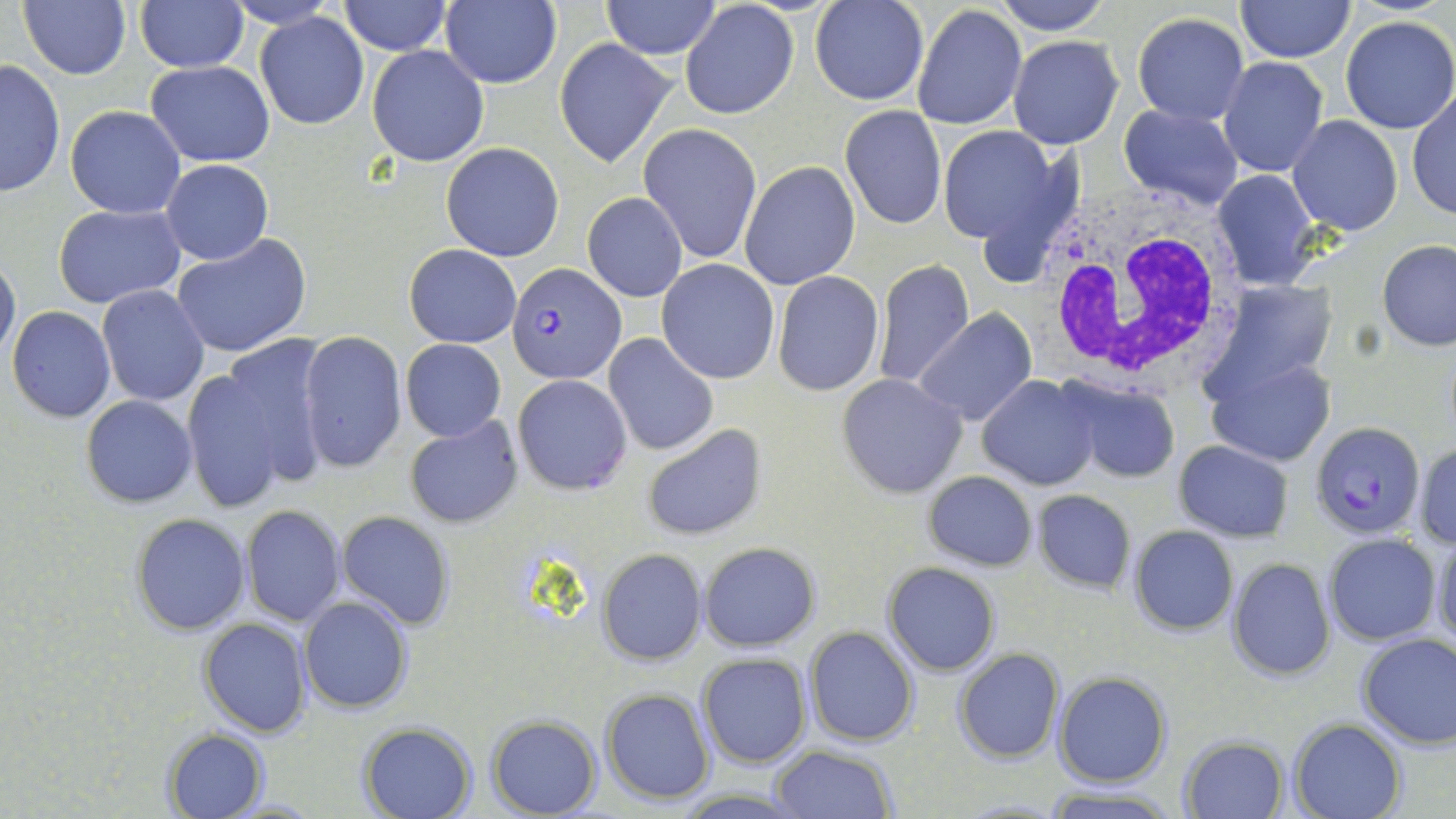
slide-level diagnosis = Plasmodium falciparum
modality = light microscopy
stain = May-Grünwald-Giemsa
field of view = one of a larger specimen
magnification = 1000x
uninfected red blood cell locations = approximate bounding boxes as (x1,y1)-(x2,y2) corner pairs in pixels: (18,0)-(131,80), (341,0)-(451,54), (439,0)-(562,89), (600,0)-(723,59), (810,0)-(928,104), (995,0)-(1112,34), (1236,0)-(1353,62), (135,1)-(249,73), (681,5)-(796,120), (912,5)-(1028,131), (1131,12)-(1248,126), (255,13)-(369,129), (1338,16)-(1456,135), (1007,36)-(1124,150), (554,39)-(676,169), (367,44)-(489,167), (1216,55)-(1329,178), (1,58)-(64,198), (147,62)-(274,165), (1406,90)-(1455,223), (1119,102)-(1244,209), (64,105)-(187,218), (840,105)-(946,230), (1287,115)-(1402,236), (637,123)-(762,263), (936,126)-(1066,248), (441,142)-(566,262), (161,159)-(272,265), (739,161)-(860,289), (1211,169)-(1323,292), (582,192)-(688,303), (53,203)-(185,309), (171,232)-(313,357), (1377,240)-(1455,351), (403,245)-(522,348), (0,253)-(20,366), (656,260)-(780,384), (872,260)-(974,391), (771,272)-(884,395), (97,284)-(208,405), (7,306)-(116,423), (913,310)-(1038,426), (299,331)-(407,474), (604,334)-(719,455), (218,337)-(333,482), (400,338)-(507,441), (1205,357)-(1336,469), (181,368)-(292,512), (512,374)-(632,495), (837,374)-(969,499), (977,375)-(1101,490), (1057,379)-(1182,484), (81,394)-(197,508), (406,416)-(524,528), (642,423)-(768,540), (1172,441)-(1295,542), (1413,442)-(1456,551), (923,471)-(1037,570), (1031,489)-(1136,594), (242,505)-(344,626), (335,511)-(456,630), (131,512)-(251,636), (1128,526)-(1238,635), (1433,532)-(1456,646), (1324,534)-(1440,644), (699,541)-(821,652), (597,548)-(707,665), (1226,558)-(1336,681), (882,562)-(1001,677), (298,595)-(413,714), (199,618)-(312,738), (805,626)-(920,747), (1356,633)-(1456,749), (954,648)-(1064,764), (696,653)-(812,768), (1053,673)-(1171,788), (601,688)-(713,804), (486,716)-(601,818), (1289,718)-(1405,819), (358,721)-(480,819), (162,727)-(270,819), (1180,736)-(1288,818), (768,746)-(898,819), (1041,786)-(1184,818)
white blood cell locations = approximate bounding boxes as (x1,y1)-(x2,y2) corner pairs in pixels: (1035,184)-(1246,389)
Plasmodium falciparum-infected red blood cell locations = approximate bounding boxes as (x1,y1)-(x2,y2) corner pairs in pixels: (508,262)-(626,386), (1311,419)-(1425,538)
preparation = thin blood film
image size = 1456×819 pixels